Classify this cell by malaria status.
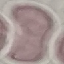
It is uninfected.

Summary:
  - Image type: cell patch, automatically extracted from a larger field of view and resized to 64 × 64 pixels
  - Capture: smartphone camera at the microscope eyepiece
  - Stain: Giemsa
  - Preparation: thin blood smear